Identify the parasite.
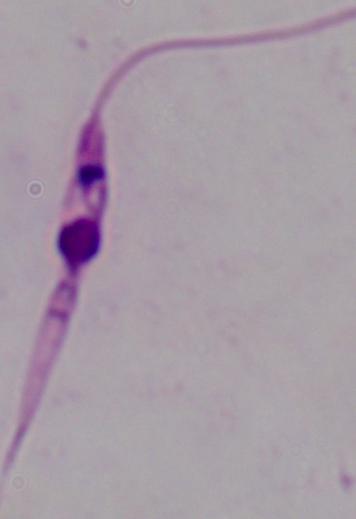

This is Leishmania.

Micrograph. 1000x magnification.